Name the parasite shown.
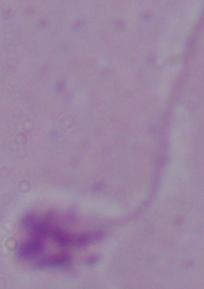
This is Leishmania.

Summary:
  - Modality: photomicrograph
  - Magnification: 1000x